Evaluate for Plasmodium parasites.
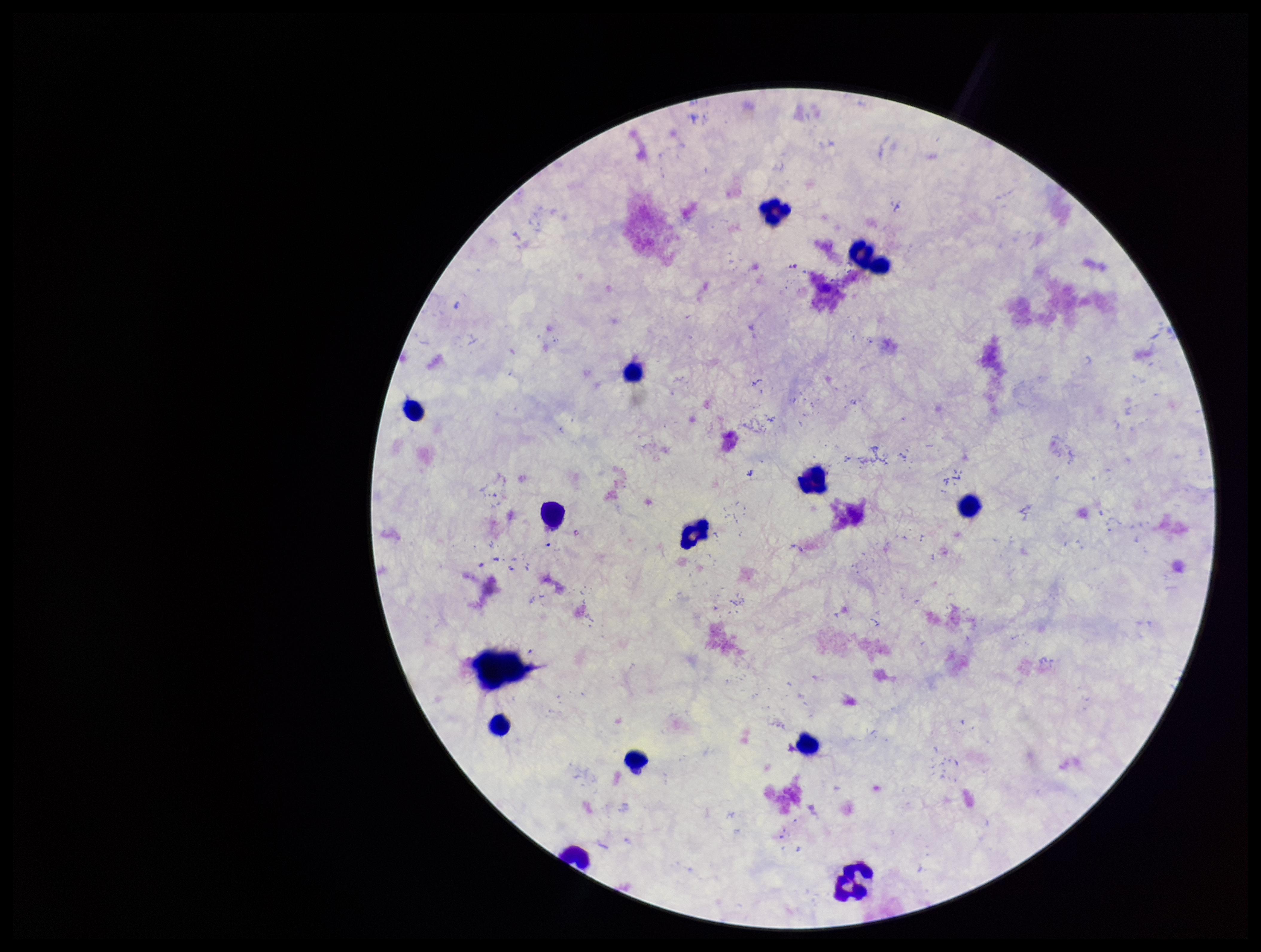
None detected.

{
  "patient_malaria_status": "negative",
  "capture": "smartphone photograph through the microscope eyepiece",
  "leukocyte_count": 13,
  "image_size": "1261×952 pixels",
  "field_of_view": "single",
  "parasite_count": 0,
  "stain": "Giemsa",
  "preparation": "thick smear"
}